Give the preparation type.
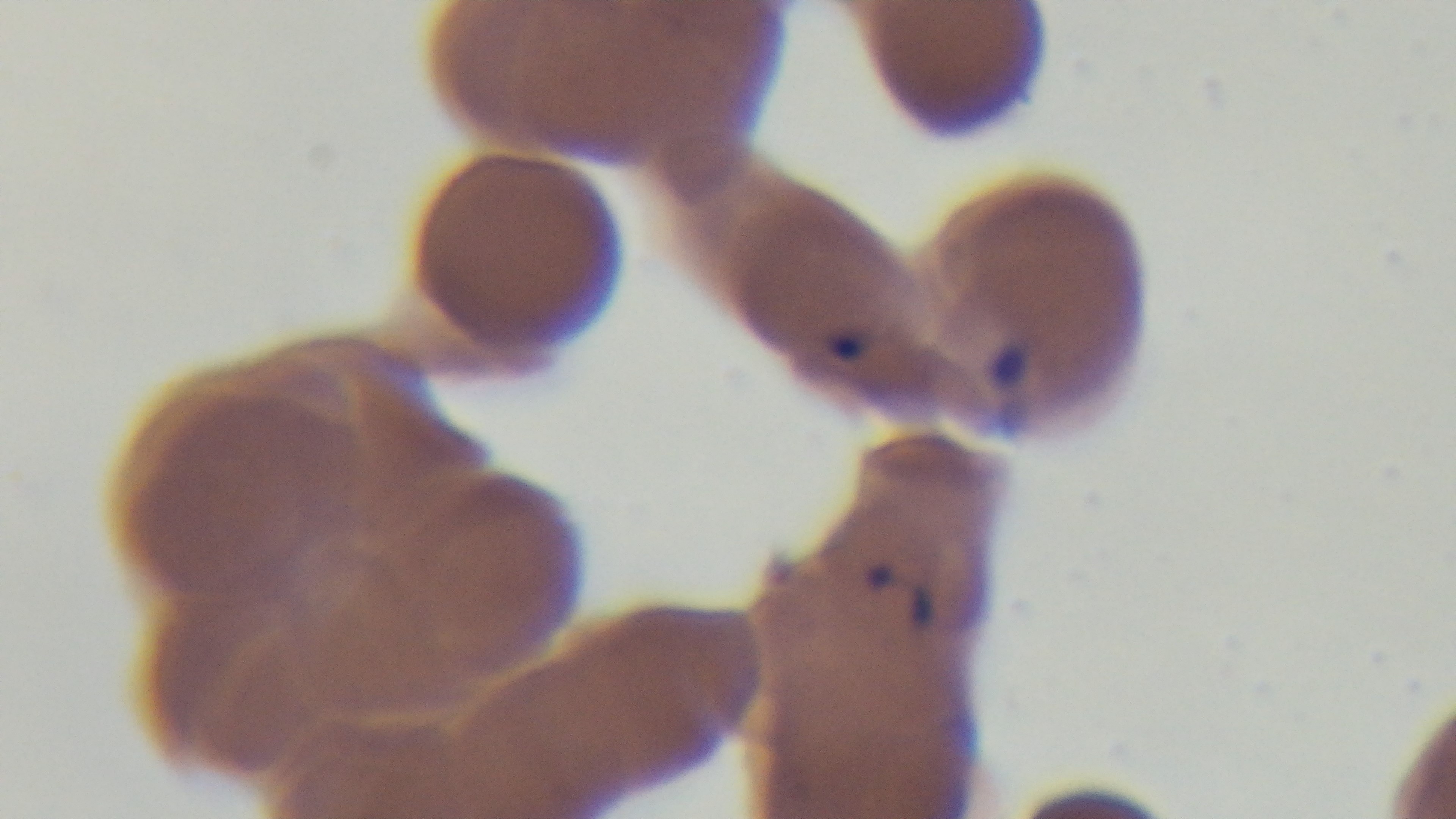

A thin smear.

Light microscopy. 100x oil-immersion objective. Single field of view. Captured with a mounted 4K digital camera. Malaria status: positive. Giemsa-stained.